Point out each leukocyte.
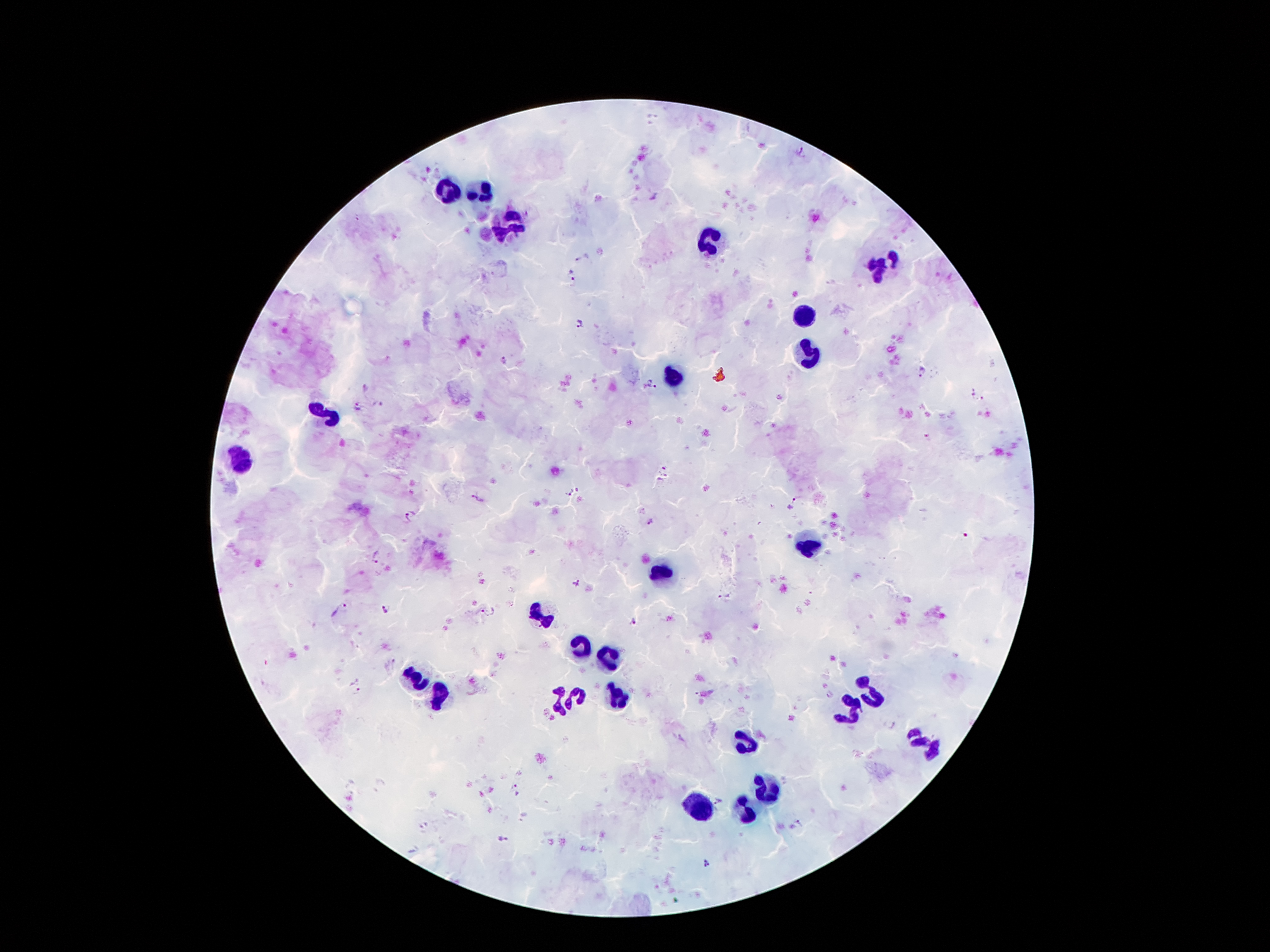

Approximate centers as (x, y) in pixels.
Leukocytes: (446, 189), (482, 191), (511, 227), (711, 239), (883, 264), (807, 313), (809, 355), (675, 376), (322, 411), (240, 458), (809, 544), (660, 571), (542, 617), (578, 646), (606, 657), (414, 676), (874, 693), (440, 697), (578, 697), (616, 697), (555, 701), (851, 709), (744, 737), (923, 741), (767, 787), (700, 806), (746, 810).

Summary:
  - Malaria parasite locations: (801, 153), (583, 257), (570, 276), (581, 323), (506, 360), (923, 372), (651, 384), (367, 389), (972, 393), (984, 402), (377, 404), (356, 408), (927, 436), (665, 472), (573, 491), (477, 499), (793, 503), (410, 516), (651, 520), (376, 555), (575, 582), (724, 596), (341, 608), (386, 608), (490, 612), (634, 621), (356, 686), (829, 696), (889, 724), (517, 788), (718, 803), (800, 821), (503, 839), (708, 863)
  - Stain: Giemsa
  - Magnification: 100x
  - Patient malaria status: positive for Plasmodium falciparum
  - Capture: smartphone camera through the microscope eyepiece
  - Image size: 1270×952 pixels
  - Field of view: single
  - Preparation: thick peripheral-blood smear